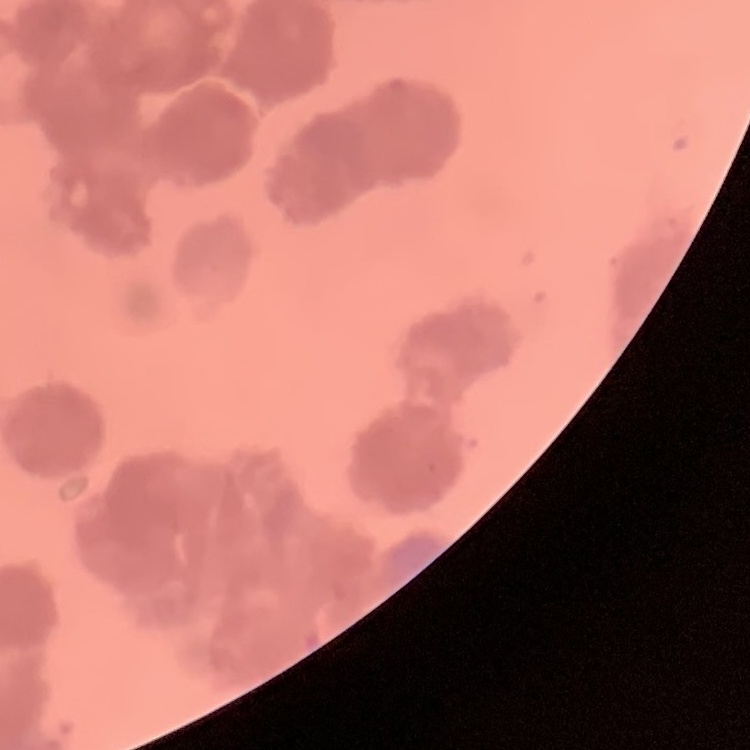
{
  "red_blood_cell_morphology": "rouleaux formation",
  "preparation": "thin blood film",
  "stain": "Field's or Giemsa",
  "image_type": "one tile cut from a larger photomicrograph"
}